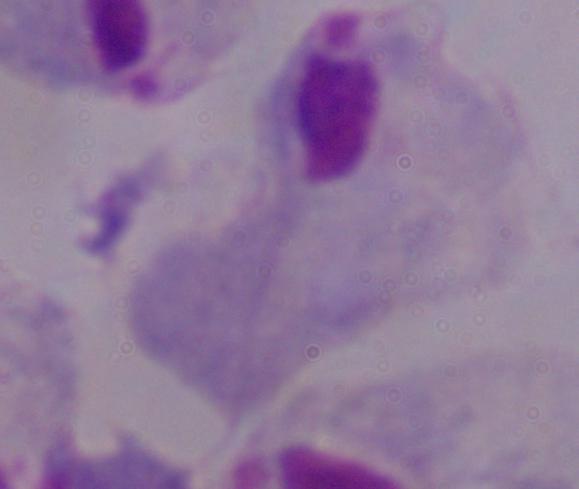

Summary:
  - Modality: photomicrograph
  - Identification: trichomonad
  - Magnification: 1000x